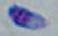

Captured at 1000x magnification. Photomicrograph. Toxoplasma gondii is shown.